Comment on the morphology of the red blood cells.
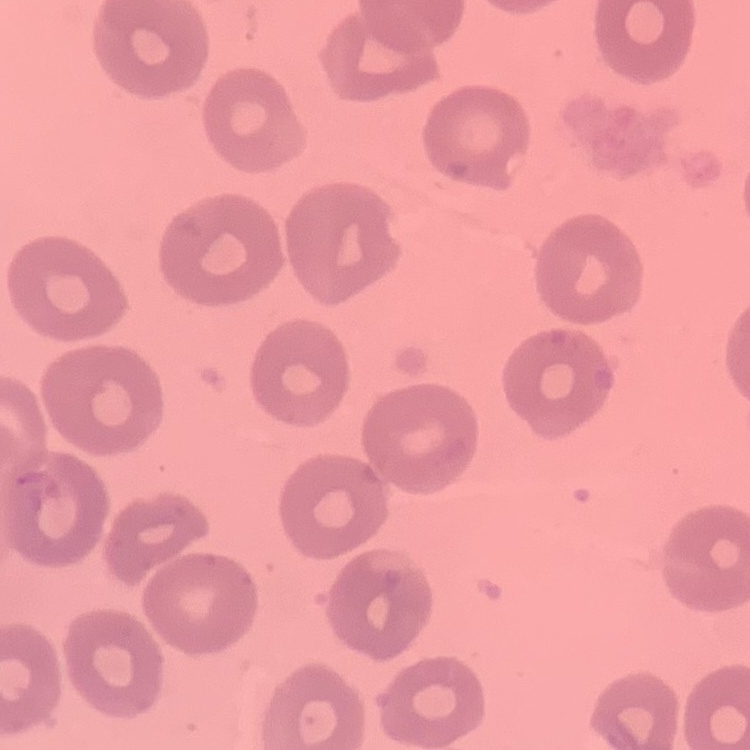
They show no rouleaux formation.

image type = one tile cut from a larger photomicrograph
stain = Field's or Giemsa
preparation = thin blood film